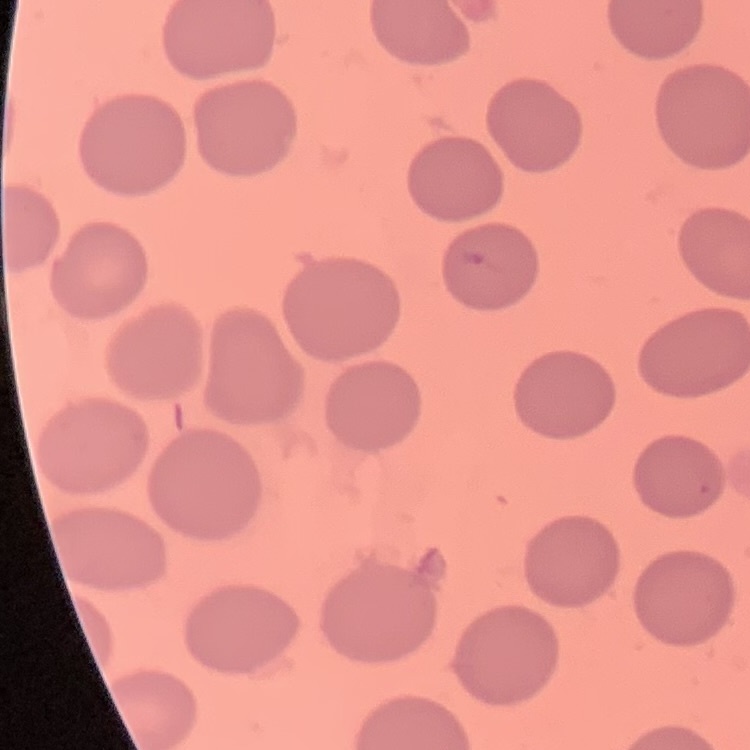
red blood cell morphology = no rouleaux formation
preparation = thin blood smear
stain = Field's or Giemsa
image type = square crop of a larger photomicrograph